Identify the parasite.
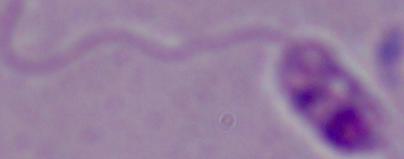
This is Leishmania.

{
  "magnification": "1000x",
  "modality": "photomicrograph"
}